State which parasite is depicted.
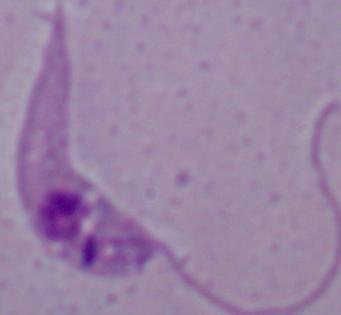
Leishmania.

Summary:
  - Modality: photomicrograph
  - Magnification: 1000x